Identify the parasite.
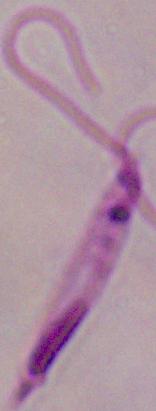
This is Leishmania.

Micrograph. Captured at 1000x magnification.